Give the extent of all white blood cells.
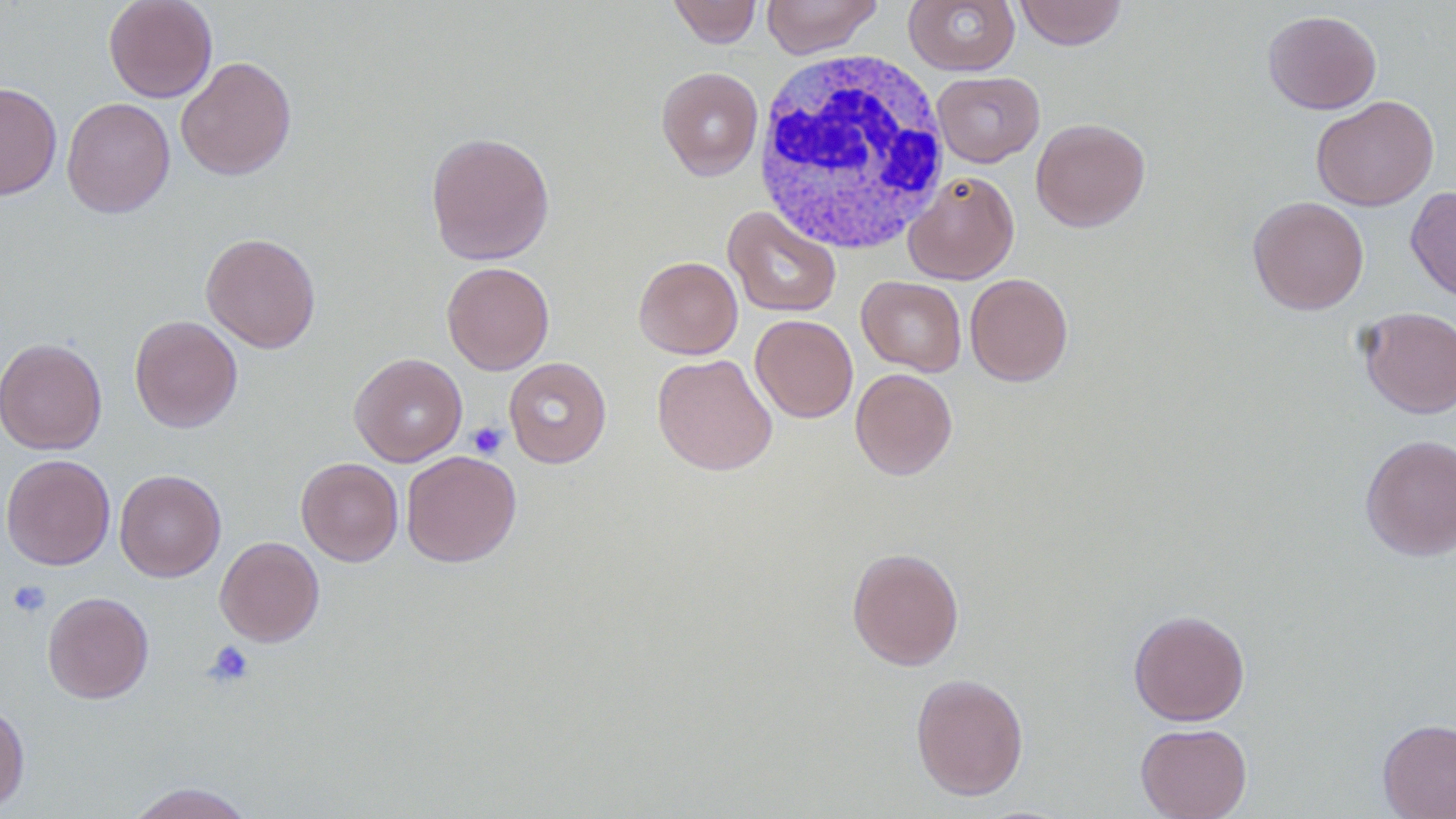
Approximate bounding boxes as (x1,y1)-(x2,y2) corner pairs in pixels.
White blood cells: (750,49)-(952,255).

Summary:
  - Uninfected red blood cell locations: (103,0)-(218,103), (668,0)-(762,48), (761,0)-(882,58), (1014,0)-(1127,50), (904,1)-(1018,75), (1263,10)-(1382,114), (176,56)-(296,181), (656,66)-(764,180), (932,71)-(1045,167), (0,81)-(62,200), (1311,95)-(1439,211), (61,97)-(175,218), (1031,117)-(1150,232), (425,130)-(555,265), (903,170)-(1020,284), (1405,186)-(1456,303), (1247,195)-(1369,315), (723,205)-(842,318), (201,232)-(321,353), (634,256)-(742,359), (441,261)-(554,374), (965,273)-(1073,386), (856,276)-(966,376), (1357,307)-(1455,418), (129,315)-(243,433), (751,315)-(858,423), (0,337)-(107,455), (349,352)-(467,466), (652,353)-(777,476), (503,357)-(612,468), (850,368)-(958,480), (1360,433)-(1456,561), (401,450)-(521,568), (1,453)-(115,570), (296,457)-(403,566), (114,469)-(226,582), (215,536)-(325,647), (846,547)-(965,671), (42,591)-(154,703), (1129,609)-(1250,726), (910,673)-(1029,800), (0,700)-(30,811), (1377,718)-(1456,818), (1136,723)-(1252,819), (124,781)-(258,819)
  - Platelet locations: (467,422)-(507,459), (7,579)-(51,618), (204,640)-(255,687)
  - Slide-level diagnosis: negative for blood parasites
  - Preparation: thin blood film
  - Image size: 1456×819 pixels
  - Magnification: 1000x
  - Field of view: one of a larger specimen
  - Modality: optical microscopy